Locate every Plasmodium falciparum parasite and identify its life-cycle stage.
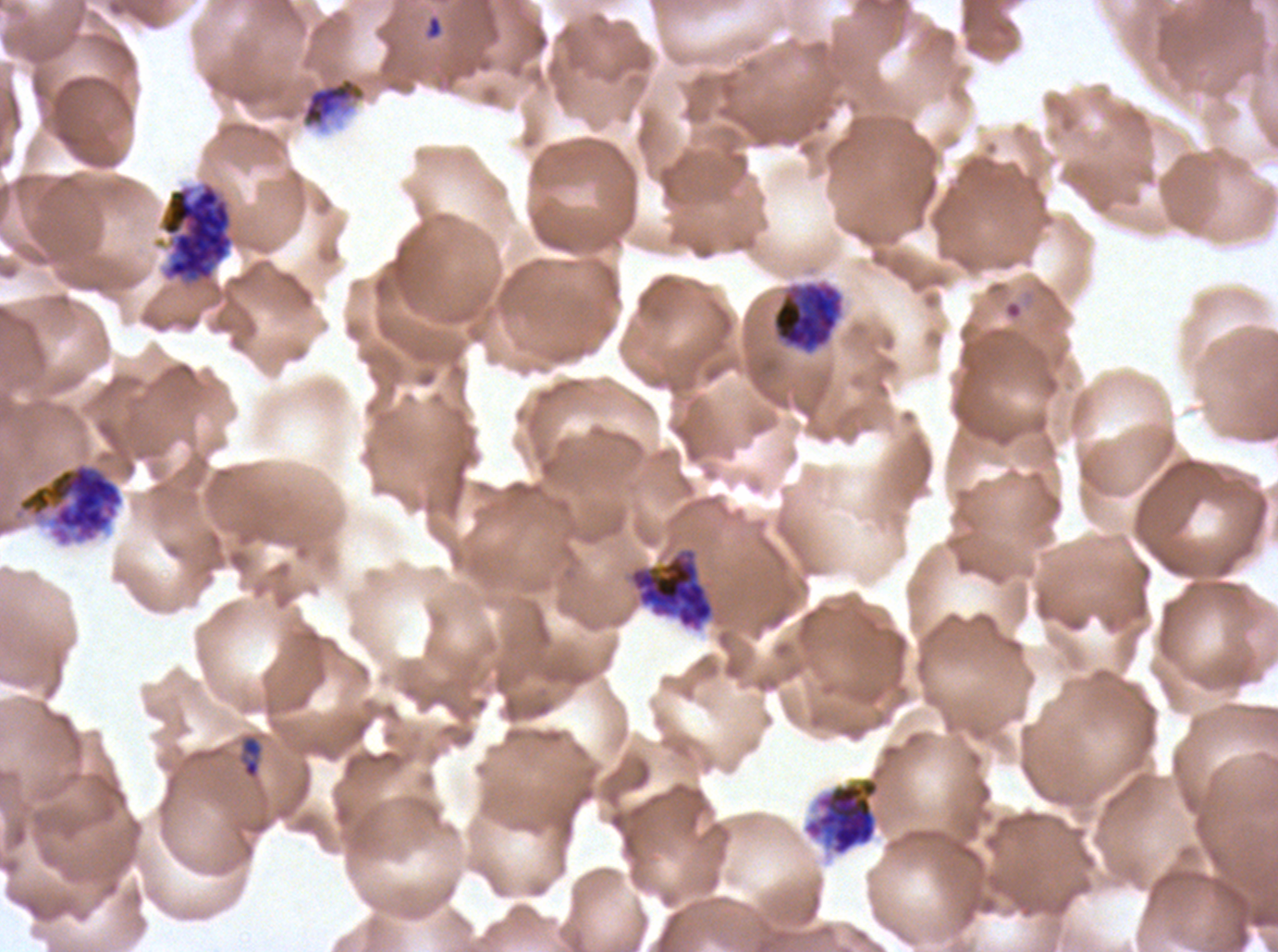

Approximate bounding boxes as [x1, y1, x2, y2] in pixels.
Rings: [424, 14, 443, 40].
Late-ring/early-trophozoite forms: [240, 735, 264, 779].
Late trophozoites: [301, 76, 366, 128].
Early schizonts: [159, 181, 234, 285], [771, 282, 843, 353], [14, 460, 125, 547], [629, 548, 715, 631], [803, 776, 880, 856].
No mid trophozoites, late schizonts, segmenters, or gametocytes observed.

Summary:
  - Preparation: thin blood smear
  - Image size: 1278×952 pixels
  - Stain: Giemsa
  - Field of view: one sub-image of a larger composite
  - Life-cycle stages observed: ring, late-ring/early-trophozoite, late trophozoite, early schizont
  - Specimen: Plasmodium falciparum from a patient in The Gambia, cultured ex vivo for 24 to 48 hours